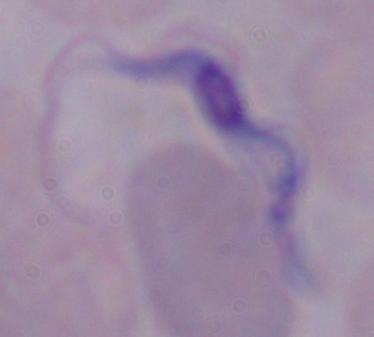
Photomicrograph. A trypanosome is seen. Captured at 1000x magnification.